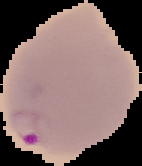

malaria status = parasitized
image size = 142×166 pixels
image type = cell region segmented out of the field of view; surrounding area masked to black
preparation = thin blood film